Assess this cell for malaria.
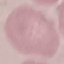

Uninfected.

stain: Giemsa
image_type: cell patch, automatically extracted from a larger field of view and resized to 64 × 64 pixels
preparation: thin blood film
capture: smartphone through the microscope eyepiece